Report the malaria status of this cell.
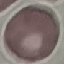

Uninfected.

Cell patch, automatically extracted from a larger field of view and resized to 64 × 64 pixels. Giemsa-stained preparation. Acquired by smartphone through the microscope eyepiece. Thin blood smear.